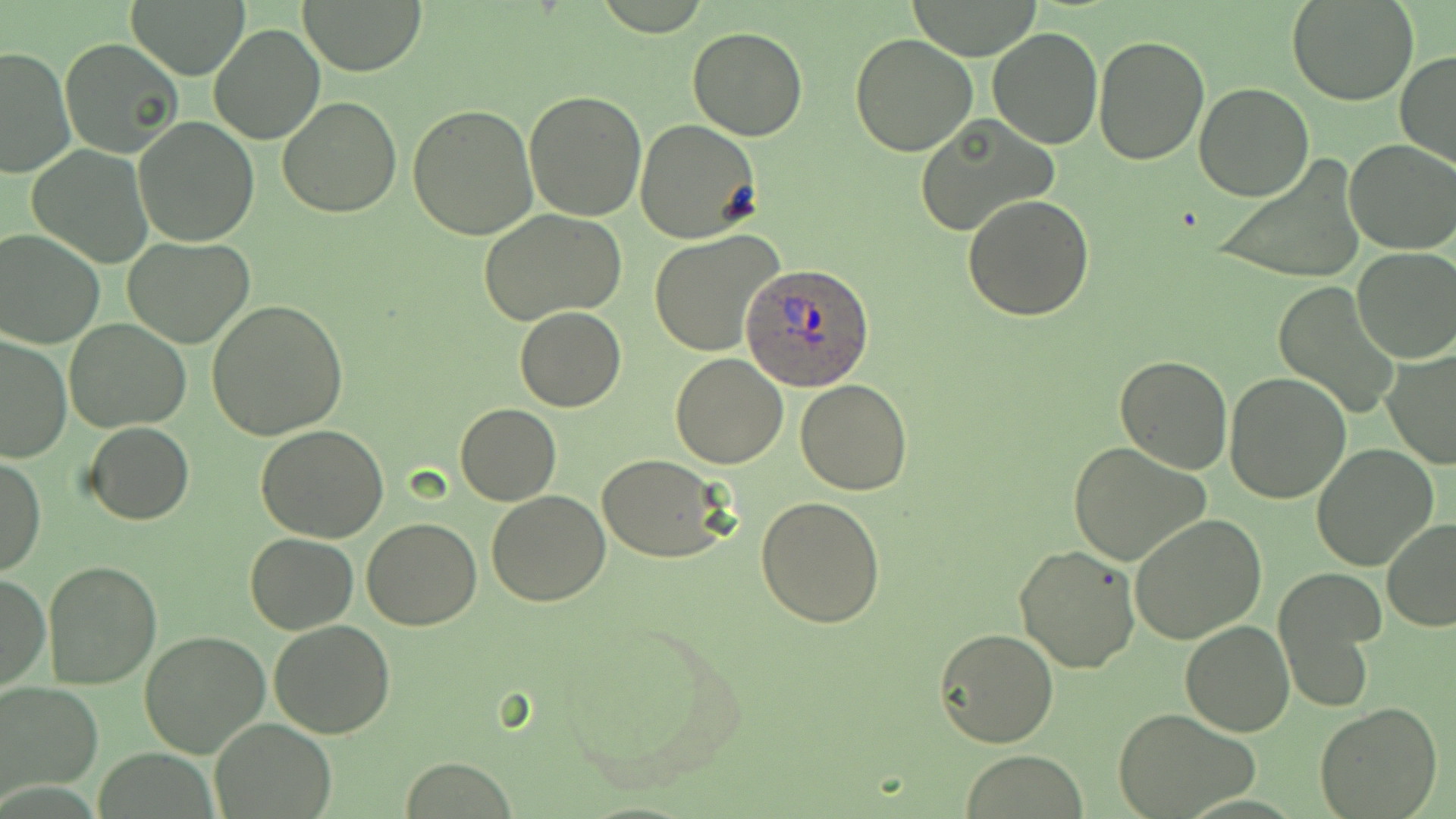

Summary:
  - Coordinate format: approximate bounding boxes as (x1, y1, x2, y2) in pixels
  - Plasmodium ovale-infected red blood cell locations: (743, 263, 875, 391)
  - Uninfected red blood cell locations: (127, 0, 251, 78), (295, 0, 429, 74), (1289, 0, 1419, 106), (901, 2, 1046, 59), (209, 23, 325, 146), (687, 26, 807, 141), (988, 26, 1103, 150), (850, 33, 979, 157), (59, 35, 182, 157), (1093, 35, 1209, 165), (0, 45, 74, 178), (1395, 50, 1456, 169), (1194, 82, 1313, 200), (524, 90, 647, 221), (277, 97, 403, 219), (407, 103, 538, 239), (135, 115, 259, 247), (913, 115, 1057, 238), (634, 119, 761, 241), (1343, 140, 1456, 255), (27, 146, 153, 266), (1211, 155, 1368, 285), (962, 193, 1095, 322), (479, 209, 630, 327), (0, 228, 105, 347), (648, 230, 786, 356), (123, 236, 255, 348), (1353, 249, 1456, 364), (1271, 282, 1400, 417), (206, 300, 349, 441), (515, 307, 626, 412), (65, 320, 190, 433), (0, 334, 74, 463), (1382, 348, 1454, 468), (669, 352, 788, 469), (1114, 356, 1234, 475), (1224, 371, 1350, 504), (795, 379, 913, 496), (455, 403, 560, 505), (84, 422, 194, 524), (255, 425, 389, 543), (1067, 442, 1211, 568), (1312, 444, 1438, 571), (1, 454, 45, 576), (597, 454, 731, 562), (485, 491, 611, 607), (756, 495, 887, 628), (1130, 515, 1267, 646), (362, 517, 482, 629), (1381, 519, 1456, 632), (246, 532, 356, 633), (1013, 544, 1141, 674), (43, 559, 162, 689), (1274, 569, 1383, 713), (0, 574, 50, 693), (268, 620, 395, 738), (1180, 620, 1294, 736), (934, 628, 1060, 748), (140, 630, 271, 758), (0, 683, 102, 800), (1313, 702, 1444, 819), (1115, 708, 1260, 818), (211, 717, 335, 818), (960, 750, 1086, 819)
  - Slide-level diagnosis: Plasmodium ovale
  - Modality: optical microscopy
  - Image size: 1456×819 pixels
  - Stain: May-Grünwald-Giemsa
  - Preparation: thin blood smear
  - Magnification: 1000x
  - Field of view: single